Locate cells.
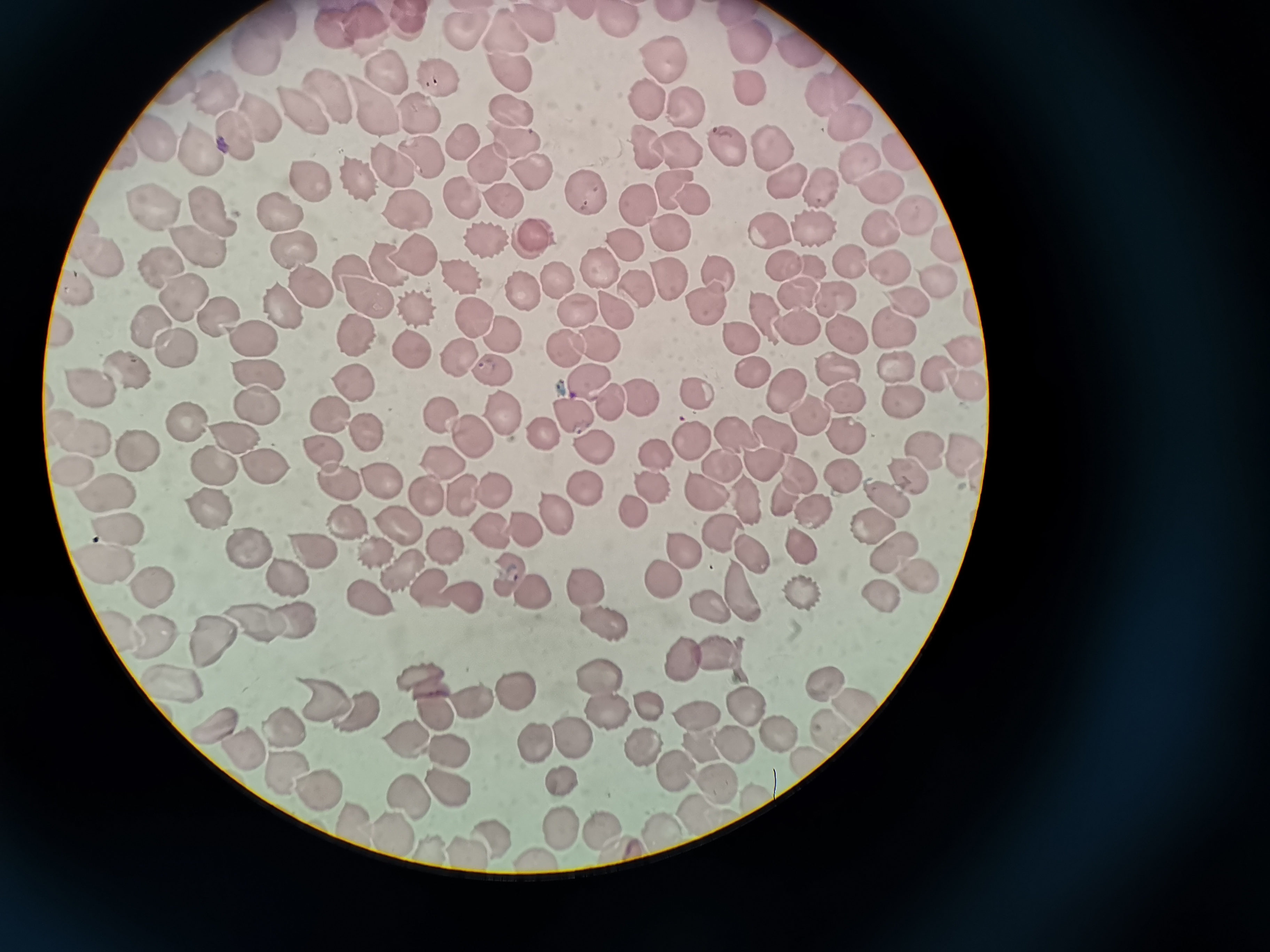
Approximate object centers, in pixels from the top-left corner.
Cells: (x=619, y=19), (x=407, y=23), (x=264, y=24), (x=360, y=25), (x=535, y=25), (x=335, y=29), (x=465, y=40), (x=508, y=40), (x=743, y=40), (x=800, y=49), (x=248, y=50), (x=660, y=59), (x=389, y=74), (x=507, y=77), (x=436, y=79), (x=746, y=87), (x=823, y=89), (x=330, y=92), (x=216, y=93), (x=646, y=100), (x=378, y=102), (x=685, y=106), (x=305, y=110), (x=508, y=110), (x=418, y=114), (x=261, y=117), (x=848, y=119), (x=154, y=137), (x=239, y=137), (x=203, y=142), (x=459, y=143), (x=651, y=145), (x=725, y=145), (x=516, y=146), (x=678, y=150), (x=770, y=152), (x=898, y=154), (x=419, y=157), (x=856, y=158), (x=487, y=159), (x=387, y=164), (x=529, y=174), (x=354, y=178), (x=780, y=179), (x=310, y=180), (x=666, y=186), (x=881, y=189), (x=819, y=191), (x=460, y=194), (x=580, y=194), (x=497, y=196), (x=693, y=197), (x=638, y=200), (x=401, y=207), (x=281, y=209), (x=210, y=210), (x=153, y=213), (x=911, y=213), (x=874, y=226), (x=765, y=229), (x=668, y=231), (x=810, y=232), (x=80, y=234), (x=484, y=241), (x=529, y=241), (x=626, y=241), (x=948, y=242), (x=288, y=244), (x=201, y=246), (x=103, y=254), (x=413, y=257), (x=386, y=262), (x=777, y=262), (x=847, y=262), (x=806, y=264), (x=345, y=267), (x=890, y=269), (x=160, y=270), (x=604, y=272), (x=557, y=274), (x=719, y=274), (x=457, y=276), (x=934, y=279), (x=672, y=281), (x=642, y=288), (x=75, y=291), (x=308, y=291), (x=797, y=292), (x=183, y=294), (x=521, y=294), (x=830, y=297), (x=364, y=298), (x=704, y=302), (x=907, y=303), (x=276, y=306), (x=578, y=308), (x=615, y=308), (x=758, y=311), (x=218, y=315), (x=473, y=317), (x=792, y=322), (x=148, y=324), (x=891, y=329), (x=61, y=331), (x=735, y=331), (x=843, y=331), (x=497, y=334), (x=243, y=336), (x=352, y=341), (x=595, y=342), (x=565, y=345), (x=172, y=347), (x=961, y=348), (x=416, y=349), (x=453, y=355), (x=837, y=368), (x=490, y=370), (x=892, y=370), (x=933, y=371), (x=119, y=372), (x=759, y=374), (x=586, y=377), (x=260, y=378), (x=353, y=383), (x=958, y=383), (x=89, y=386), (x=779, y=388), (x=637, y=391), (x=843, y=392), (x=605, y=396), (x=693, y=398), (x=902, y=398), (x=254, y=405), (x=568, y=408), (x=806, y=411), (x=326, y=412), (x=440, y=414), (x=507, y=414), (x=184, y=422), (x=365, y=427), (x=552, y=431), (x=770, y=431), (x=736, y=432), (x=235, y=434), (x=471, y=434), (x=84, y=435), (x=845, y=439), (x=588, y=441), (x=688, y=443), (x=917, y=449), (x=139, y=450), (x=327, y=451), (x=654, y=455), (x=959, y=458), (x=760, y=459), (x=722, y=461), (x=442, y=462), (x=263, y=463), (x=65, y=466), (x=214, y=466), (x=841, y=469), (x=794, y=470), (x=906, y=473), (x=376, y=479), (x=339, y=482), (x=577, y=485), (x=705, y=486), (x=488, y=487), (x=647, y=487), (x=106, y=490), (x=425, y=493), (x=781, y=493), (x=880, y=494), (x=741, y=497), (x=459, y=498), (x=620, y=502), (x=811, y=506), (x=550, y=512), (x=209, y=513), (x=865, y=521), (x=485, y=522), (x=350, y=523), (x=516, y=524), (x=393, y=527), (x=119, y=528), (x=724, y=529), (x=438, y=542), (x=799, y=545), (x=307, y=547), (x=685, y=547), (x=885, y=548), (x=374, y=549), (x=247, y=550), (x=752, y=553), (x=99, y=556), (x=405, y=568), (x=507, y=571), (x=915, y=573), (x=277, y=574), (x=662, y=574), (x=151, y=581), (x=584, y=584), (x=432, y=588), (x=800, y=588), (x=737, y=591), (x=457, y=592), (x=530, y=592), (x=876, y=592), (x=374, y=595), (x=702, y=607), (x=251, y=619), (x=300, y=619), (x=596, y=621), (x=113, y=628), (x=208, y=633), (x=149, y=636), (x=714, y=650), (x=678, y=659), (x=423, y=675), (x=822, y=682), (x=167, y=683), (x=595, y=683), (x=506, y=684), (x=314, y=698), (x=468, y=698), (x=844, y=700), (x=647, y=702), (x=736, y=707), (x=600, y=708), (x=694, y=709), (x=352, y=711), (x=434, y=713), (x=215, y=723), (x=824, y=727), (x=277, y=728), (x=764, y=729), (x=569, y=735), (x=400, y=738), (x=534, y=738), (x=692, y=739), (x=727, y=739), (x=445, y=746), (x=645, y=749), (x=239, y=750), (x=804, y=762), (x=280, y=769), (x=678, y=770), (x=557, y=776), (x=445, y=782), (x=313, y=787), (x=710, y=787), (x=407, y=790), (x=757, y=794), (x=690, y=818), (x=349, y=820), (x=555, y=822), (x=602, y=828), (x=488, y=829), (x=390, y=830), (x=655, y=832), (x=435, y=845), (x=616, y=850), (x=461, y=851), (x=534, y=855).

{
  "image_size": "1270×952 pixels",
  "capture": "smartphone camera at the microscope eyepiece",
  "preparation": "thin blood smear",
  "field_of_view": "single",
  "stain": "Giemsa"
}